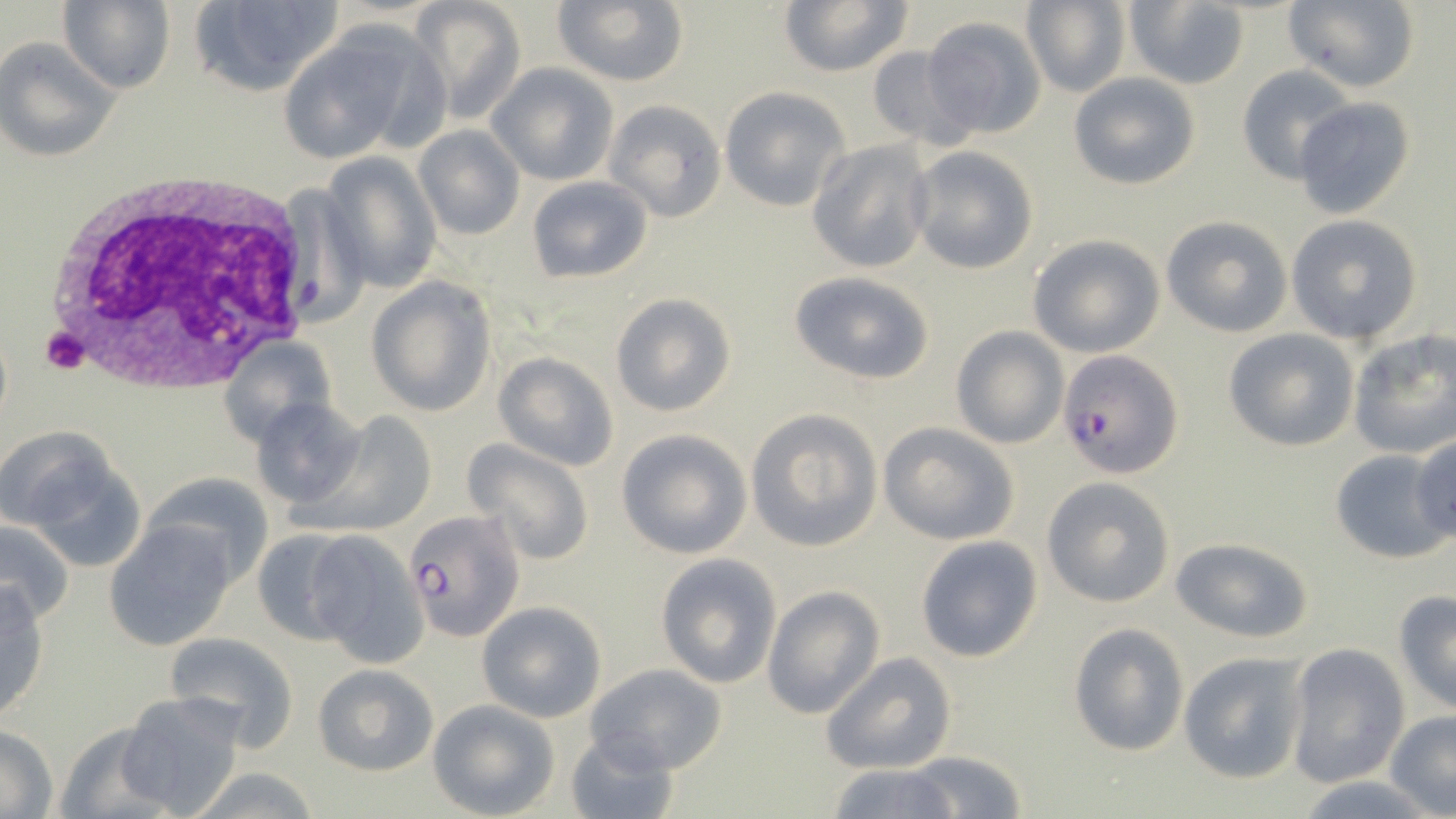

Summary:
  - Coordinate format: approximate bounding boxes as [x1, y1, x2, y2] in pixels
  - Uninfected red blood cell locations: [60, 0, 176, 94], [553, 0, 689, 87], [777, 0, 914, 78], [1284, 0, 1420, 92], [189, 1, 342, 98], [411, 1, 528, 124], [1019, 1, 1130, 96], [1122, 1, 1249, 89], [920, 14, 1048, 140], [276, 22, 444, 166], [0, 35, 122, 162], [866, 46, 976, 153], [487, 63, 619, 187], [1236, 66, 1356, 184], [1068, 72, 1202, 191], [719, 85, 852, 212], [1293, 96, 1416, 219], [603, 99, 728, 223], [412, 125, 525, 240], [806, 139, 935, 275], [906, 146, 1039, 276], [321, 152, 442, 293], [525, 175, 654, 284], [1160, 215, 1291, 337], [1286, 215, 1423, 344], [1026, 233, 1166, 358], [787, 270, 938, 385], [367, 278, 496, 415], [611, 293, 735, 417], [950, 326, 1067, 449], [1224, 328, 1359, 452], [1348, 330, 1456, 459], [218, 336, 335, 445], [492, 351, 620, 471], [248, 396, 366, 511], [306, 409, 439, 536], [745, 409, 883, 552], [879, 421, 1021, 545], [614, 429, 751, 559], [1410, 435, 1456, 544], [464, 439, 594, 567], [14, 440, 146, 567], [1329, 450, 1446, 564], [142, 472, 271, 585], [1042, 476, 1176, 607], [0, 518, 76, 625], [103, 518, 241, 651], [251, 528, 363, 647], [307, 532, 429, 665], [914, 534, 1045, 663], [1169, 536, 1316, 642], [654, 554, 781, 687], [0, 580, 52, 722], [764, 585, 884, 718], [1393, 591, 1456, 715], [477, 601, 608, 720], [1066, 621, 1191, 757], [164, 631, 300, 750], [1284, 642, 1412, 789], [1178, 650, 1311, 784], [822, 652, 957, 774], [584, 661, 729, 775], [312, 664, 438, 777], [112, 693, 247, 818], [428, 700, 558, 817], [1385, 710, 1456, 817], [51, 721, 182, 819], [0, 726, 58, 816], [565, 731, 678, 819], [903, 752, 1030, 818], [822, 762, 965, 819], [182, 767, 323, 819], [1289, 775, 1442, 818]
  - White blood cell locations: [38, 163, 317, 392]
  - Plasmodium falciparum-infected red blood cell locations: [1058, 350, 1185, 478], [402, 509, 524, 642]
  - Platelet locations: [41, 327, 89, 374]
  - Slide-level diagnosis: Plasmodium falciparum
  - Preparation: thin blood film
  - Modality: light microscopy
  - Magnification: 1000x
  - Stain: May-Grünwald-Giemsa
  - Field of view: single
  - Image size: 1456×819 pixels